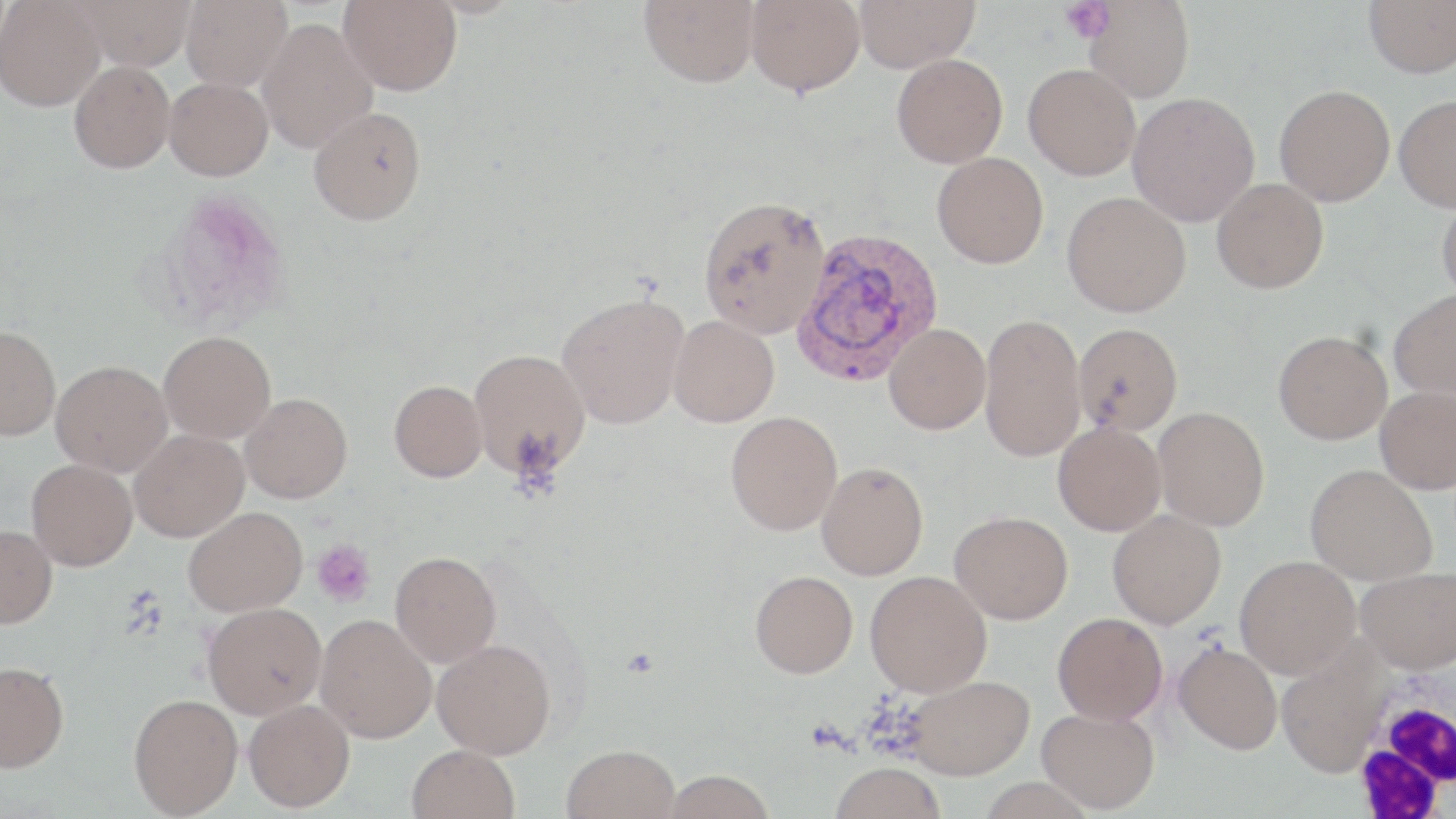
slide-level diagnosis = Plasmodium vivax
modality = optical microscopy
white blood cell locations = approximate bounding boxes as [x1, y1, x2, y2] in pixels: [1352, 673, 1453, 815]
platelet locations = approximate bounding boxes as [x1, y1, x2, y2] in pixels: [1059, 0, 1115, 43], [312, 539, 376, 607]
preparation = thin blood film
stain = May-Grünwald-Giemsa
magnification = 1000x
Plasmodium vivax-infected red blood cell locations = approximate bounding boxes as [x1, y1, x2, y2] in pixels: [789, 226, 944, 387]
field of view = single
uninfected red blood cell locations = approximate bounding boxes as [x1, y1, x2, y2] in pixels: [0, 0, 106, 111], [72, 0, 195, 71], [181, 0, 292, 92], [338, 0, 463, 96], [638, 0, 760, 88], [746, 0, 865, 96], [853, 0, 980, 72], [1362, 0, 1456, 78], [1084, 1, 1194, 102], [257, 18, 378, 153], [892, 53, 1008, 167], [69, 60, 175, 173], [1023, 63, 1140, 180], [164, 77, 273, 180], [1274, 85, 1395, 206], [1127, 92, 1260, 226], [1394, 94, 1456, 212], [308, 106, 426, 225], [932, 152, 1049, 268], [1211, 178, 1329, 294], [1062, 191, 1191, 317], [697, 195, 831, 338], [1436, 196, 1456, 304], [1388, 289, 1456, 403], [557, 293, 689, 428], [979, 313, 1086, 462], [668, 315, 779, 427], [1072, 322, 1183, 435], [884, 323, 991, 434], [0, 325, 60, 440], [1273, 330, 1392, 444], [159, 331, 276, 442], [469, 348, 591, 480], [50, 360, 172, 476], [389, 380, 487, 481], [1375, 386, 1456, 494], [240, 393, 352, 503], [1153, 406, 1270, 531], [725, 411, 842, 535], [1053, 423, 1166, 535], [129, 430, 249, 542], [26, 459, 137, 571], [816, 462, 928, 580], [1304, 464, 1438, 585], [183, 507, 308, 616], [1107, 509, 1226, 628], [950, 511, 1073, 624], [0, 524, 57, 629], [390, 551, 501, 667], [1235, 555, 1360, 678], [1355, 567, 1456, 673], [750, 570, 858, 678], [865, 570, 992, 696], [203, 602, 326, 719], [1052, 612, 1168, 725], [315, 614, 437, 743], [432, 639, 556, 759], [1174, 642, 1283, 754], [0, 660, 69, 772], [903, 675, 1034, 779], [129, 693, 243, 816], [243, 699, 355, 812], [1036, 707, 1160, 813], [562, 744, 680, 819], [407, 745, 520, 819], [830, 762, 945, 819], [662, 769, 776, 818]
image size = 1456×819 pixels